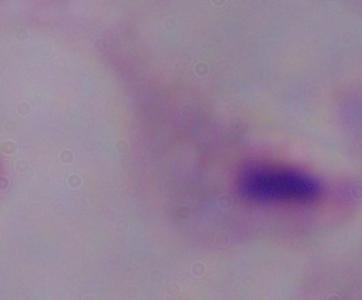 A trichomonad is seen. Micrograph. Captured at 1000x magnification.